Identify the cell.
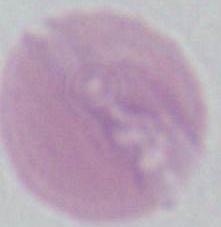
This is an erythrocyte.

Summary:
  - Modality: micrograph
  - Magnification: 1000x